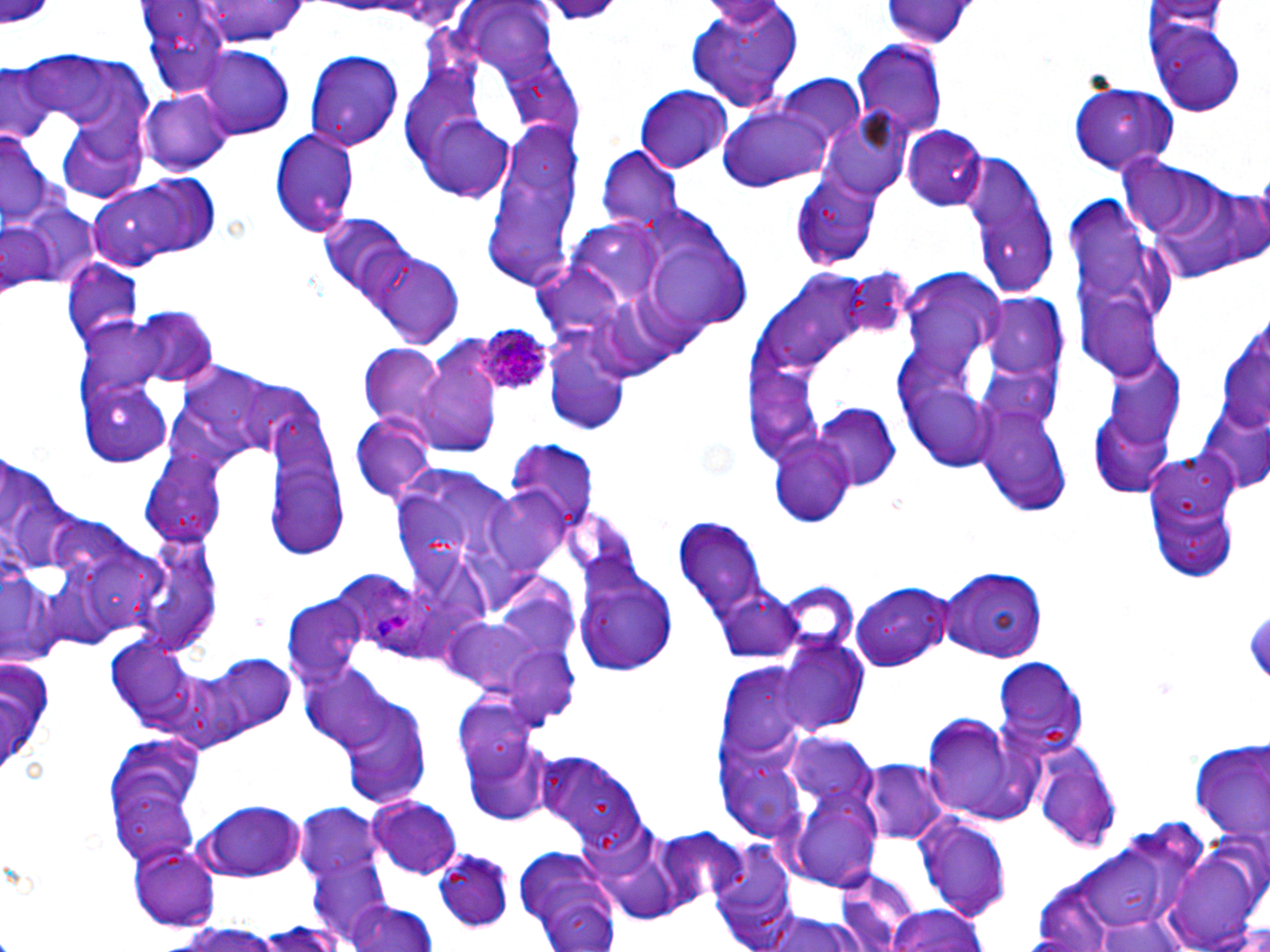

{
  "slide_level_diagnosis": "Plasmodium ovale",
  "uninfected_red_blood_cell_locations": "approximate bounding boxes as (x1,y1)-(x2,y2) corner pairs in pixels: (0,0)-(57,30), (192,0)-(311,49), (541,0)-(622,24), (880,0)-(977,48), (687,1)-(803,114), (1150,2)-(1228,43), (140,4)-(236,91), (473,8)-(563,80), (1150,20)-(1247,116), (851,39)-(947,139), (195,47)-(293,137), (305,48)-(405,150), (1,67)-(51,144), (775,75)-(866,146), (1070,83)-(1180,175), (635,86)-(733,171), (140,90)-(231,176), (720,106)-(832,193), (820,110)-(913,200), (420,117)-(517,201), (55,122)-(151,200), (902,125)-(988,211), (484,126)-(580,293), (269,128)-(358,236), (0,132)-(59,234), (596,148)-(684,231), (1117,152)-(1268,283), (962,154)-(1058,299), (90,175)-(222,269), (1066,195)-(1178,384), (11,197)-(103,292), (319,214)-(411,300), (651,243)-(737,334), (361,248)-(466,348), (63,260)-(143,349), (981,297)-(1070,385), (123,307)-(219,385), (542,339)-(631,437), (358,344)-(448,432), (410,349)-(503,460), (78,378)-(173,466), (976,397)-(1074,516), (263,403)-(344,561), (815,405)-(903,489), (1087,406)-(1177,498), (350,415)-(436,503), (768,439)-(858,525), (507,442)-(596,539), (1138,450)-(1246,585), (140,455)-(230,547), (390,459)-(520,586), (0,461)-(78,575), (484,486)-(574,577), (674,514)-(771,622), (134,535)-(221,654), (936,565)-(1048,659), (0,567)-(55,665), (331,568)-(421,652), (578,568)-(680,677), (490,575)-(579,659), (850,581)-(956,673), (772,582)-(859,660), (713,585)-(803,664), (285,598)-(366,684), (1247,608)-(1270,679), (773,639)-(867,738), (105,640)-(200,734), (195,654)-(299,744), (994,659)-(1089,754), (300,661)-(397,755), (721,663)-(808,761), (453,695)-(540,781), (337,697)-(433,805), (920,714)-(1045,826), (462,729)-(557,828), (787,730)-(879,813), (103,734)-(205,866), (1188,741)-(1263,846), (1036,748)-(1124,850), (535,751)-(646,848), (720,756)-(812,843), (864,757)-(950,846), (789,787)-(883,889), (367,795)-(464,876), (196,799)-(310,880), (297,805)-(383,887), (913,810)-(1013,923), (651,826)-(748,915), (598,837)-(686,925), (711,838)-(800,945), (513,843)-(622,951), (128,844)-(222,930), (1070,848)-(1177,926), (1167,850)-(1264,950), (432,852)-(515,931), (309,859)-(395,944), (833,870)-(923,951), (343,900)-(439,952), (885,905)-(989,952), (755,911)-(878,952), (1090,912)-(1193,952), (168,920)-(288,951)",
  "magnification": "1000x",
  "plasmodium_ovale_infected_red_blood_cell_locations": "approximate bounding boxes as (x1,y1)-(x2,y2) corner pairs in pixels: (476,326)-(553,394)",
  "image_size": "1270×952 pixels",
  "preparation": "thin blood smear",
  "stain": "May-Grünwald-Giemsa",
  "modality": "optical microscopy",
  "field_of_view": "single"
}